State the blood parasite species.
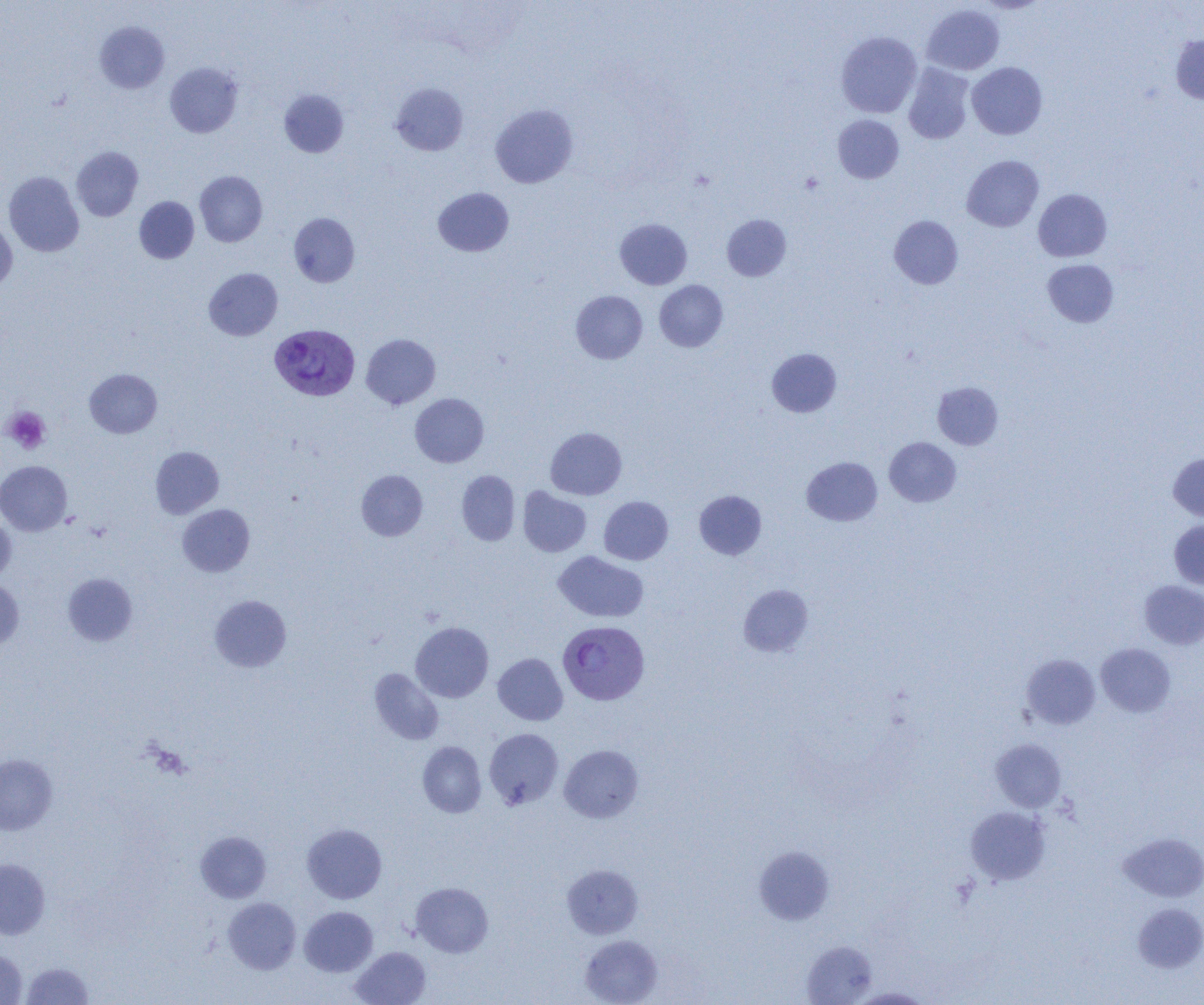
Plasmodium vivax.

Approximate bounding boxes as (x1,y1)-(x2,y2) corner pairs in pixels. Uninfected red blood cell locations: (922,4)-(1005,75), (94,21)-(169,93), (836,31)-(922,118), (1171,34)-(1204,103), (165,62)-(243,138), (967,62)-(1047,139), (903,63)-(975,144), (391,82)-(468,155), (279,89)-(349,157), (490,104)-(578,188), (833,114)-(904,183), (72,146)-(144,221), (962,155)-(1044,231), (195,170)-(267,247), (4,171)-(84,256), (433,187)-(514,256), (1033,189)-(1112,262), (134,196)-(199,263), (289,212)-(360,287), (722,214)-(791,281), (889,215)-(963,289), (614,218)-(692,289), (0,220)-(17,291), (1042,259)-(1119,327), (204,268)-(282,340), (654,280)-(728,352), (570,290)-(648,363), (361,334)-(440,409), (767,348)-(841,417), (85,369)-(162,438), (932,382)-(1004,450), (410,393)-(489,467), (546,427)-(627,500), (884,437)-(961,506), (150,446)-(224,518), (1168,453)-(1204,521), (802,457)-(882,526), (0,460)-(72,535), (356,470)-(427,541), (456,470)-(520,545), (518,487)-(591,557), (694,490)-(766,560), (599,496)-(673,565), (177,504)-(255,577), (0,514)-(16,584), (1169,520)-(1204,590), (553,551)-(649,622), (62,573)-(137,645), (0,580)-(24,650), (1139,580)-(1204,649), (739,585)-(813,657), (210,594)-(292,672), (411,622)-(493,702), (1096,643)-(1175,717), (493,653)-(568,725), (1021,653)-(1100,729), (369,668)-(444,745), (484,728)-(563,809), (990,738)-(1067,812), (417,741)-(486,817), (559,744)-(643,822), (0,754)-(57,835), (965,806)-(1051,885), (302,823)-(387,904), (195,831)-(271,903), (1119,832)-(1204,902), (753,845)-(835,925), (0,859)-(50,939), (562,864)-(643,939), (411,882)-(493,957), (223,897)-(301,974), (1133,904)-(1204,973), (299,906)-(378,976), (580,935)-(662,1005), (801,940)-(877,1004), (350,946)-(431,1005), (0,949)-(27,1004), (22,961)-(93,1004), (851,987)-(934,1004). Platelet locations: (2,407)-(51,454). Plasmodium vivax-infected red blood cell locations: (269,324)-(360,401), (558,620)-(650,705). Image is 1204×1005 pixels. Thin blood film. Light microscopy. One field of a larger specimen. 1000x magnification.